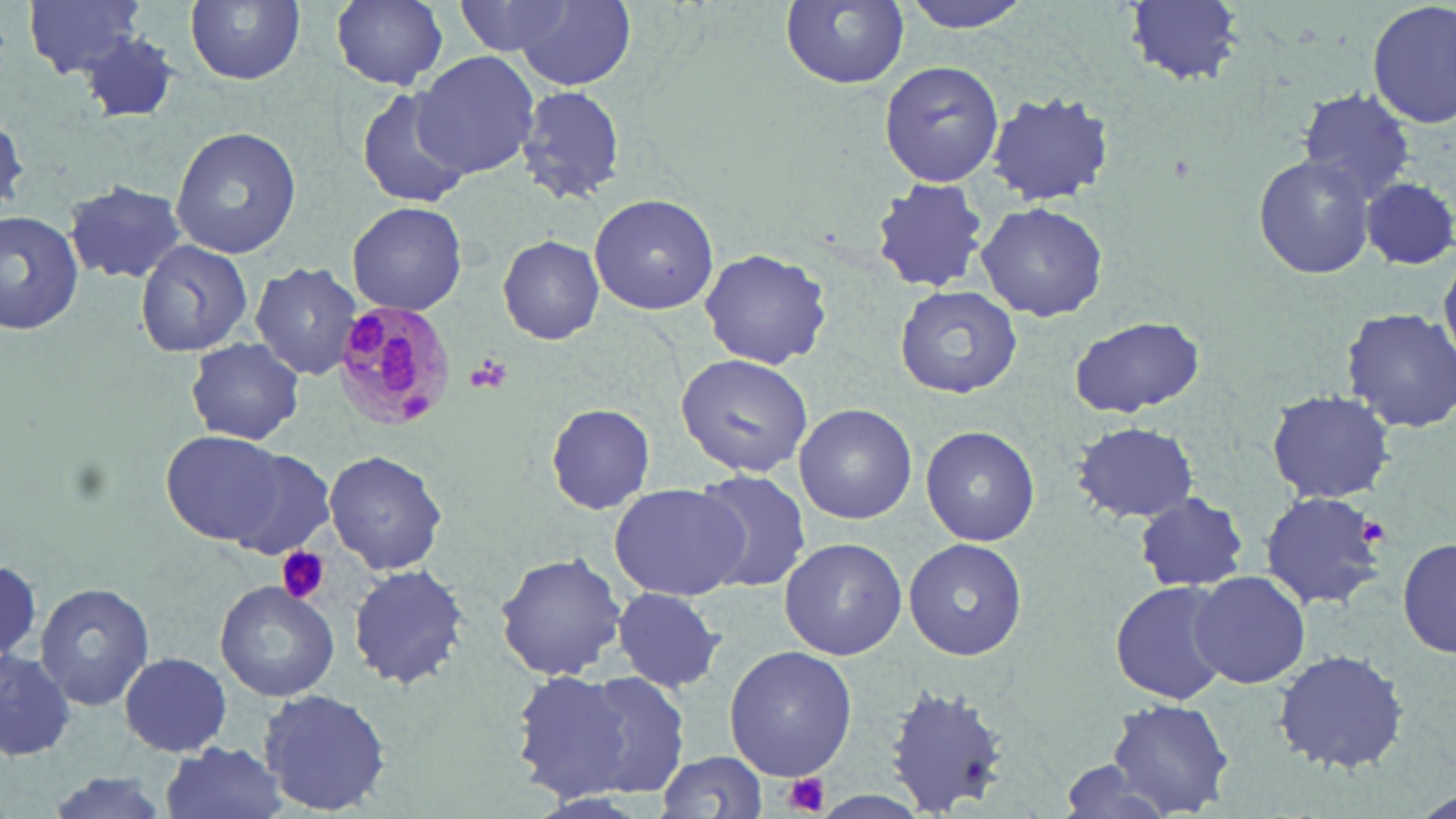

slide_level_diagnosis: Plasmodium malariae
stain: May-Grünwald-Giemsa
magnification: 1000x
modality: optical microscopy
image_size: 1456×819 pixels
preparation: thin blood smear
plasmodium_malariae_infected_red_blood_cell_locations: 'approximate bounding boxes as (x1, y1, x2, y2) in pixels: (330, 295, 458, 431)'
platelet_locations: 'approximate bounding boxes as (x1, y1, x2, y2) in pixels: (465, 356, 511, 397), (1360, 515, 1389, 543), (276, 548, 330, 604), (781, 772, 830, 817)'
field_of_view: one of a larger specimen
uninfected_red_blood_cell_locations: 'approximate bounding boxes as (x1, y1, x2, y2) in pixels: (21, 0, 151, 81), (185, 0, 305, 85), (458, 0, 581, 55), (512, 0, 638, 94), (898, 0, 1039, 33), (1125, 0, 1244, 86), (1368, 0, 1454, 130), (328, 1, 451, 91), (780, 1, 909, 88), (75, 31, 183, 125), (415, 51, 542, 178), (879, 61, 1004, 186), (516, 84, 624, 205), (356, 86, 472, 208), (1296, 87, 1417, 202), (984, 91, 1116, 206), (170, 127, 301, 258), (1253, 154, 1375, 281), (1359, 174, 1456, 271), (871, 179, 989, 294), (64, 181, 188, 284), (589, 193, 719, 314), (347, 200, 467, 314), (975, 201, 1108, 321), (0, 212, 83, 334), (498, 234, 605, 345), (136, 237, 254, 357), (698, 248, 833, 370), (250, 261, 362, 382), (895, 285, 1023, 398), (1341, 308, 1456, 433), (1068, 314, 1204, 419), (186, 339, 303, 445), (676, 353, 811, 477), (1267, 390, 1394, 502), (546, 403, 657, 516), (794, 403, 916, 525), (1072, 421, 1200, 524), (921, 425, 1040, 546), (162, 431, 293, 544), (323, 449, 448, 575), (688, 468, 810, 593), (609, 482, 750, 600), (1259, 491, 1387, 610), (1135, 492, 1248, 591), (780, 537, 908, 660), (904, 537, 1028, 661), (1397, 537, 1456, 660), (495, 550, 626, 682), (348, 564, 473, 689), (1187, 569, 1311, 687), (1110, 576, 1235, 703), (216, 580, 339, 702), (37, 581, 153, 710), (609, 585, 728, 693), (724, 646, 857, 779), (1272, 649, 1411, 772), (2, 651, 77, 759), (117, 653, 235, 756), (511, 669, 630, 799), (578, 672, 690, 798), (883, 683, 1011, 814), (258, 687, 391, 816), (1105, 702, 1237, 817), (160, 741, 291, 818), (655, 750, 770, 817), (1052, 761, 1183, 817), (35, 771, 184, 819)'